Identify the parasite.
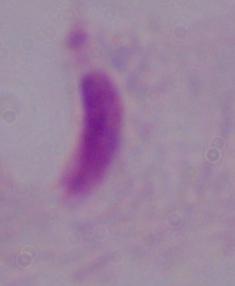

A trichomonad.

Summary:
  - Magnification: 1000x
  - Modality: micrograph